Classify this cell by malaria status.
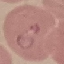
It is parasitized.

Cell patch, automatically extracted from a larger field of view and resized to 64 × 64 pixels. Giemsa-stained preparation. Acquired by smartphone through the microscope eyepiece. Thin blood film.